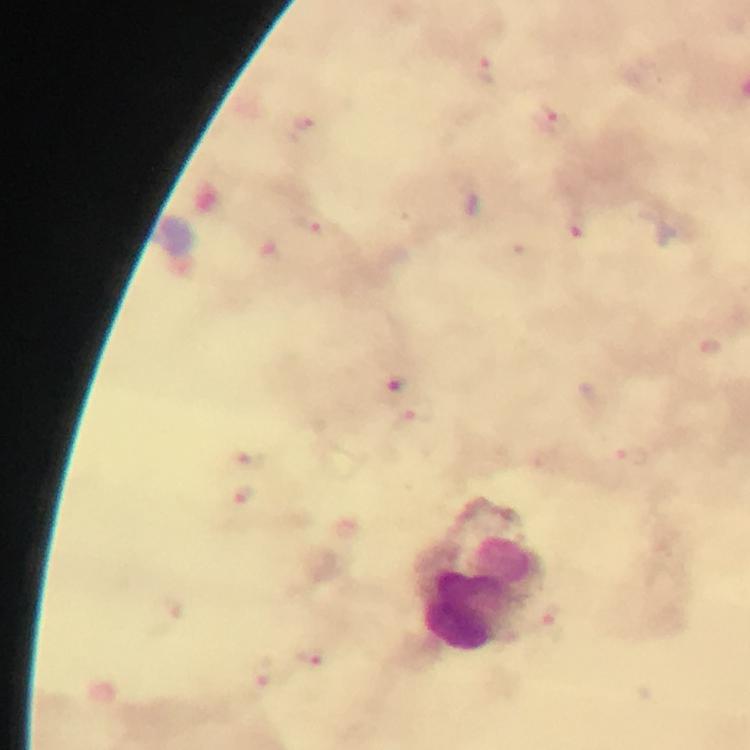

{
  "image_size": "750×750 pixels",
  "capture": "smartphone mounted on the microscope",
  "stain": "Giemsa",
  "cropped_from": "one field of view",
  "preparation": "thick smear",
  "leukocyte_locations": "approximate centers as {x, y} in pixels: {508, 566}, {465, 608}",
  "malaria_parasite_locations": "approximate centers as {x, y} in pixels: {552, 118}, {305, 122}, {312, 225}, {574, 225}, {398, 382}, {245, 495}, {310, 655}, {264, 677}",
  "immersion_oil": "applied",
  "context": "from a diagnostic examination for malaria",
  "magnification": "100x"
}